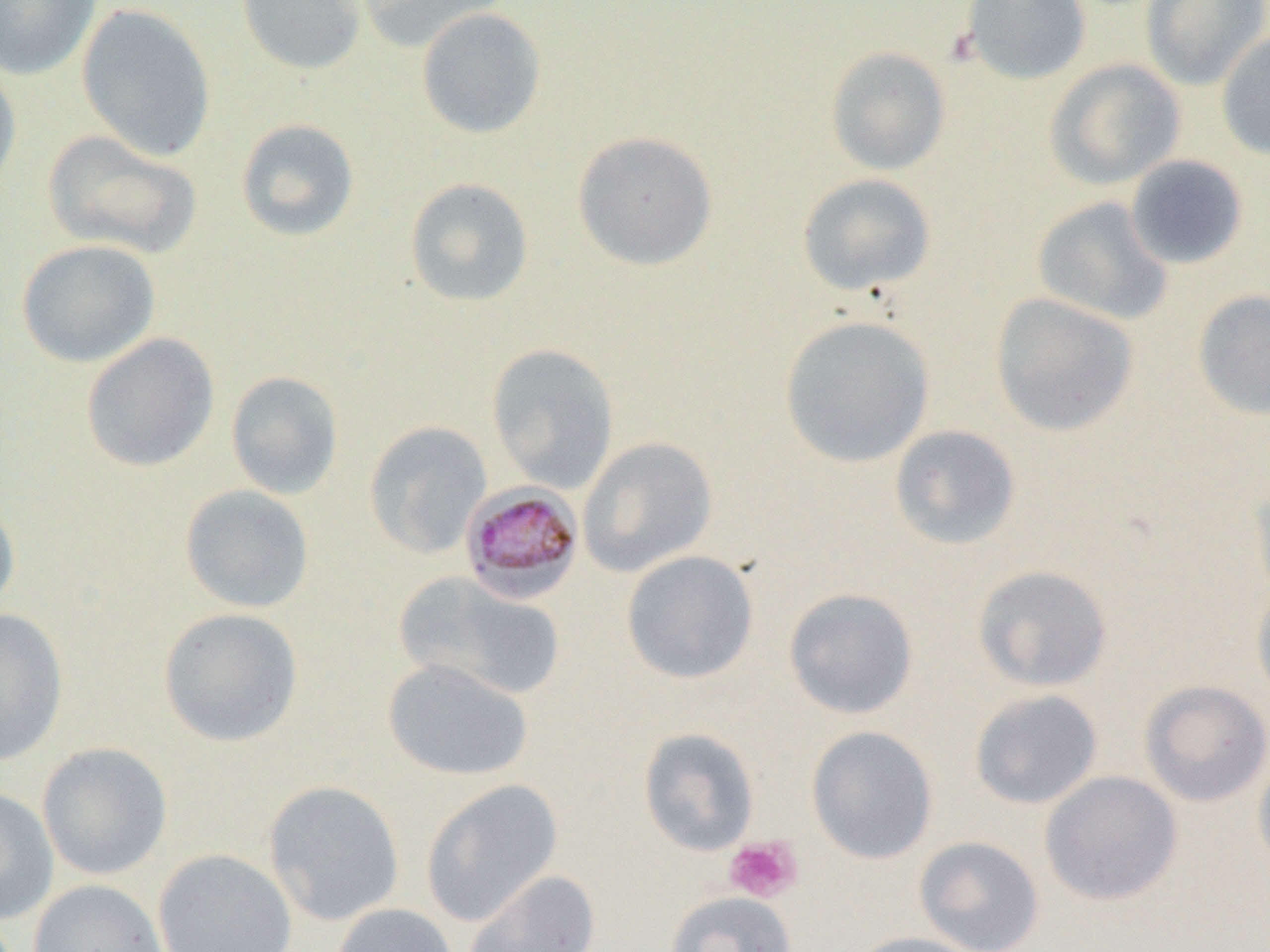

Summary:
  - Coordinate format: approximate bounding boxes as [x1, y1, x2, y2] in pixels
  - Uninfected red blood cell locations: [0, 0, 102, 80], [237, 0, 367, 75], [355, 0, 513, 53], [960, 0, 1092, 85], [1140, 0, 1269, 91], [76, 3, 217, 162], [416, 7, 547, 139], [1216, 30, 1270, 160], [825, 45, 952, 176], [1045, 58, 1186, 190], [0, 60, 22, 201], [235, 118, 360, 242], [42, 129, 203, 260], [572, 130, 718, 271], [1124, 155, 1249, 270], [797, 173, 936, 297], [404, 177, 534, 308], [1032, 196, 1174, 326], [16, 239, 161, 368], [1192, 289, 1270, 420], [990, 292, 1139, 437], [779, 315, 936, 468], [80, 332, 220, 472], [486, 342, 619, 494], [225, 370, 343, 499], [364, 421, 493, 559], [889, 424, 1021, 550], [577, 437, 717, 577], [1249, 475, 1270, 604], [180, 484, 315, 613], [0, 498, 21, 617], [621, 550, 759, 684], [972, 564, 1113, 692], [395, 571, 566, 701], [1251, 582, 1270, 709], [783, 587, 919, 720], [158, 607, 304, 747], [0, 608, 68, 766], [382, 658, 533, 781], [1138, 679, 1270, 807], [969, 689, 1103, 809], [807, 726, 938, 864], [638, 727, 760, 856], [36, 742, 173, 880], [1253, 746, 1270, 881], [1040, 770, 1183, 906], [422, 779, 562, 926], [264, 780, 405, 927], [0, 787, 59, 925], [914, 836, 1044, 952], [153, 848, 297, 952], [462, 869, 601, 952], [28, 879, 170, 952], [665, 891, 796, 952], [332, 903, 457, 952], [845, 931, 986, 952]
  - Plasmodium malariae-infected red blood cell locations: [460, 483, 584, 605]
  - Platelet locations: [724, 836, 802, 903]
  - Slide-level diagnosis: Plasmodium malariae
  - Modality: light microscopy
  - Image size: 1270×952 pixels
  - Field of view: single
  - Preparation: thin blood film
  - Magnification: 1000x